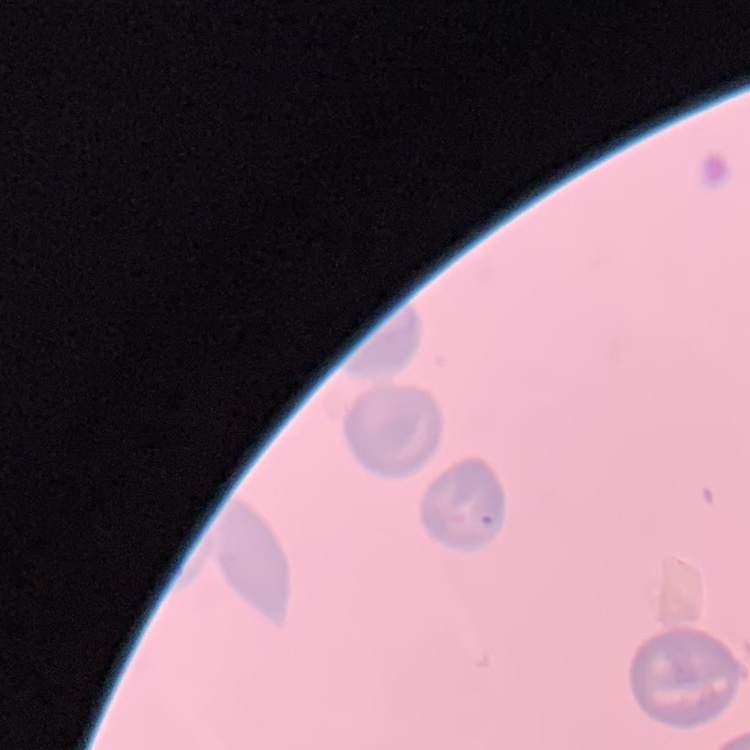 The red blood cells show no rouleaux formation. Thin peripheral smear. Field's or Giemsa stain. One tile cut from a larger photomicrograph.